Describe the morphology of the red blood cells.
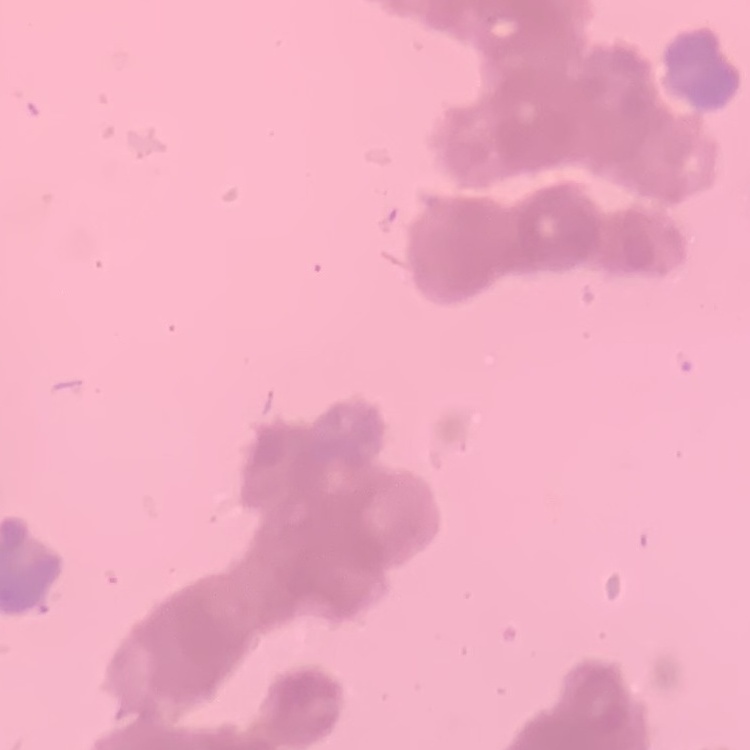
They show rouleaux formation.

preparation = thin peripheral smear
image type = one tile cut from a larger photomicrograph
stain = Field's or Giemsa